Report the malaria status of this cell.
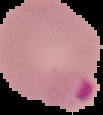

Parasitized.

Summary:
  - Image type: segmented cell region with the area outside set to black
  - Image size: 103×115 pixels
  - Preparation: thin blood smear